Assess the morphology of the red blood cells.
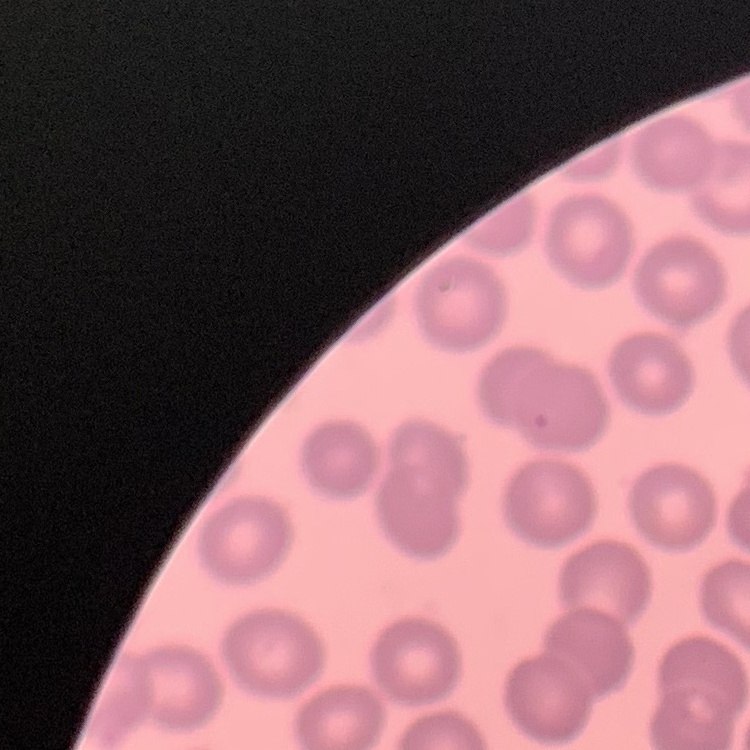

No rouleaux formation.

Square crop of a larger photomicrograph. Stained with either Field's or Giemsa. Thin blood smear.